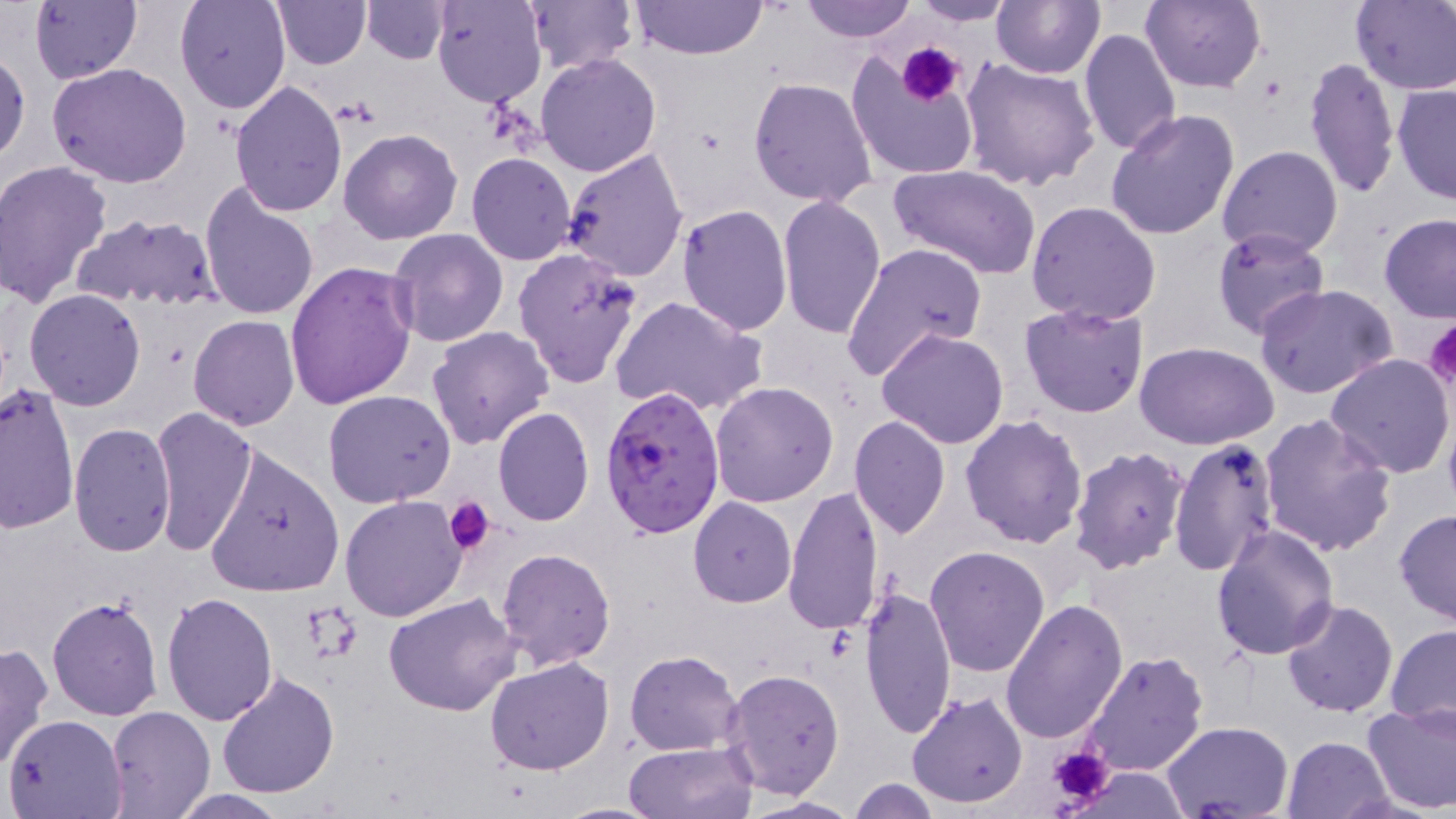 Approximate bounding boxes as (x1, y1, x2, y2) in pixels. Plasmodium falciparum-infected red blood cell locations: (601, 385, 727, 539). Platelet locations: (898, 43, 965, 105), (1422, 320, 1456, 394), (444, 496, 496, 555), (1044, 743, 1113, 810). Uninfected red blood cell locations: (29, 0, 141, 86), (174, 0, 291, 114), (273, 0, 371, 70), (360, 0, 451, 64), (429, 0, 546, 109), (522, 0, 637, 75), (631, 0, 768, 62), (797, 0, 918, 43), (991, 0, 1104, 79), (1141, 0, 1266, 92), (1351, 0, 1456, 92), (908, 1, 1017, 25), (1080, 28, 1181, 158), (1, 51, 29, 164), (535, 53, 662, 175), (846, 54, 979, 182), (1304, 56, 1401, 200), (960, 57, 1099, 192), (48, 62, 192, 188), (748, 77, 877, 207), (229, 79, 346, 217), (1392, 82, 1455, 206), (1107, 110, 1241, 244), (337, 129, 463, 245), (562, 145, 689, 282), (1216, 145, 1345, 261), (466, 152, 576, 265), (1, 161, 114, 309), (888, 164, 1042, 280), (200, 183, 320, 321), (776, 195, 888, 341), (1026, 200, 1161, 326), (677, 204, 793, 335), (73, 213, 223, 315), (1378, 215, 1456, 321), (1212, 228, 1330, 340), (388, 229, 508, 347), (840, 242, 988, 381), (513, 247, 644, 389), (284, 261, 418, 409), (1256, 283, 1398, 401), (23, 289, 146, 410), (610, 296, 768, 418), (1018, 301, 1150, 419), (188, 315, 300, 431), (426, 326, 553, 448), (876, 329, 1010, 449), (1135, 342, 1281, 451), (1325, 353, 1456, 480), (0, 381, 79, 532), (710, 381, 840, 506), (322, 390, 456, 508), (151, 406, 256, 555), (493, 408, 595, 526), (959, 413, 1089, 547), (1258, 413, 1397, 557), (848, 416, 950, 539), (67, 421, 177, 558), (1169, 439, 1279, 575), (205, 444, 344, 597), (1067, 445, 1189, 576), (783, 484, 885, 636), (339, 494, 470, 623), (688, 498, 797, 607), (1393, 508, 1456, 627), (1209, 524, 1339, 660), (924, 546, 1050, 679), (495, 547, 616, 669), (860, 586, 957, 740), (163, 591, 278, 726), (384, 595, 521, 716), (46, 596, 163, 721), (1001, 597, 1128, 744), (1281, 599, 1397, 718), (1384, 624, 1456, 731), (0, 642, 53, 771), (1080, 648, 1209, 777), (626, 650, 743, 754), (484, 656, 615, 775), (722, 670, 844, 797), (216, 671, 340, 799), (906, 690, 1029, 809), (1363, 702, 1456, 817), (105, 707, 214, 818), (4, 713, 126, 818), (1163, 721, 1293, 816), (1282, 736, 1395, 819), (623, 740, 758, 819), (847, 777, 947, 818), (166, 791, 293, 818), (740, 795, 863, 818), (554, 801, 667, 817). Slide-level diagnosis: Plasmodium falciparum. One field of a larger specimen. Thin blood smear. 1000x magnification. May-Grünwald-Giemsa stain. Image is 1456×819 pixels. Light microscopy.